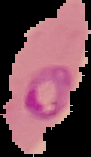

Summary:
  - Preparation: thin blood film
  - Image type: segmented cell region on a black background
  - Image size: 91×157 pixels
  - Result: malaria parasites detected